Assess this cell for malaria.
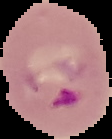
It is parasitized.

image_size: 112×139 pixels
preparation: thin blood smear
image_type: cell region segmented out of the field of view; surrounding area masked to black